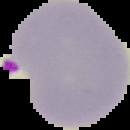

Summary:
  - Image type: segmented cell region with the area outside set to black
  - Malaria status: parasitized
  - Image size: 130×130 pixels
  - Preparation: thin blood film